Locate and identify every blood parasite.
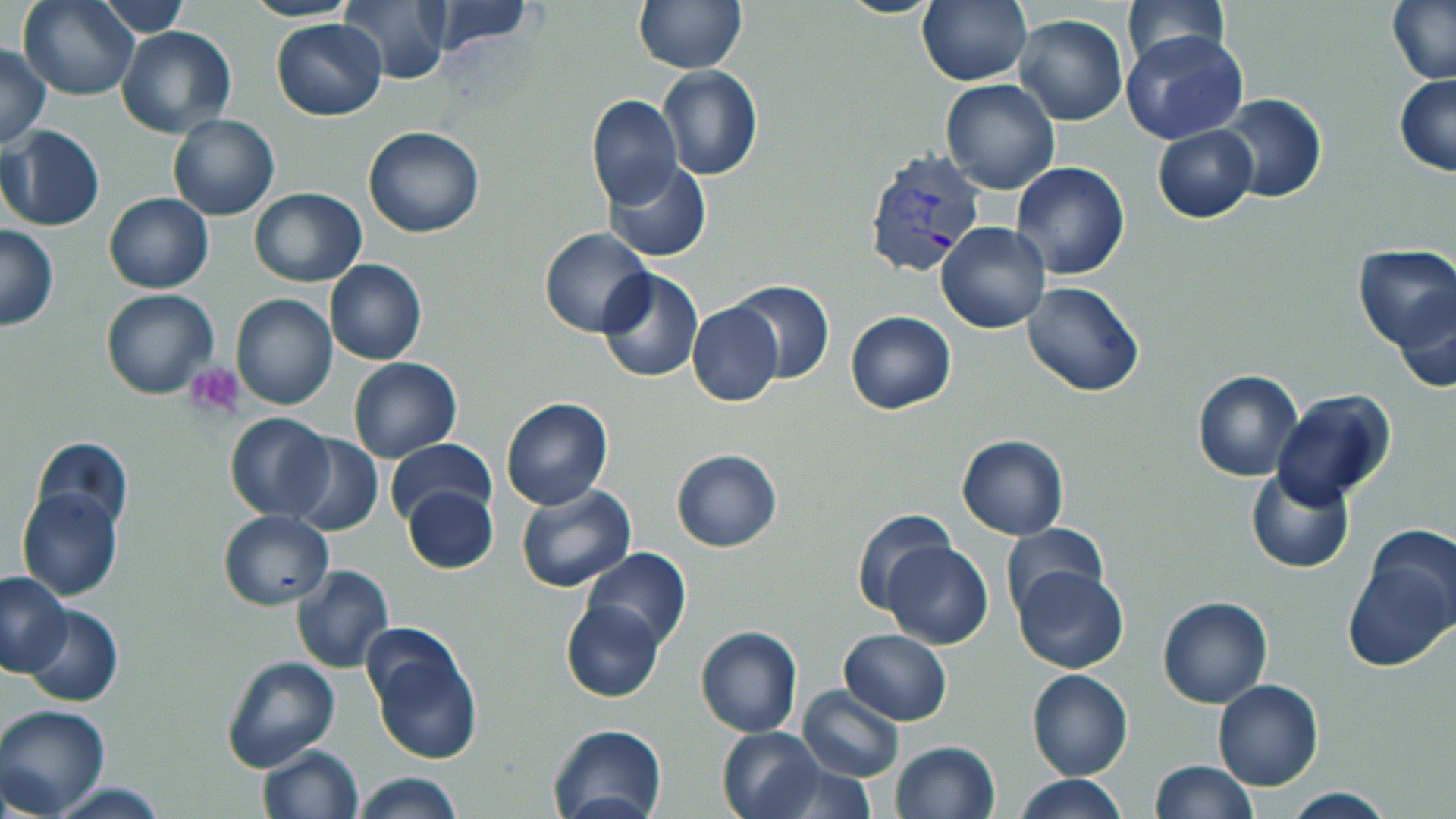

Approximate bounding boxes as (x1,y1)-(x2,y2) corner pairs in pixels.
Plasmodium vivax-infected red blood cells: (859,150)-(984,280).
No Plasmodium falciparum, Plasmodium ovale, Plasmodium malariae, Babesia divergens, or Trypanosoma brucei observed.

slide_level_diagnosis: Plasmodium vivax
magnification: 1000x
field_of_view: single
modality: light microscopy
preparation: thin blood film
uninfected_red_blood_cell_locations: 'approximate bounding boxes as (x1,y1)-(x2,y2) corner pairs in pixels: (20,0)-(140,100), (98,0)-(193,35), (243,0)-(359,24), (338,0)-(450,84), (835,0)-(944,18), (917,0)-(1031,86), (1122,0)-(1228,69), (1388,0)-(1456,86), (420,1)-(534,57), (633,1)-(745,73), (1014,13)-(1127,126), (271,18)-(387,121), (116,26)-(237,139), (1123,29)-(1248,145), (0,45)-(50,149), (658,65)-(763,181), (1395,75)-(1456,177), (940,77)-(1060,196), (1212,93)-(1327,203), (585,94)-(684,209), (168,114)-(279,221), (1152,124)-(1258,223), (1,125)-(104,233), (363,125)-(486,238), (604,159)-(712,263), (1011,161)-(1130,280), (248,187)-(367,286), (103,193)-(213,293), (935,222)-(1051,334), (0,225)-(58,331), (539,228)-(653,338), (1353,245)-(1456,351), (325,258)-(427,365), (596,268)-(704,383), (729,279)-(834,384), (1023,282)-(1145,399), (1394,288)-(1456,394), (101,289)-(218,399), (231,293)-(338,410), (686,302)-(782,406), (845,310)-(956,416), (347,358)-(461,462), (1192,369)-(1304,482), (1271,390)-(1397,505), (500,396)-(613,510), (224,414)-(335,522), (287,434)-(383,537), (957,435)-(1069,540), (30,436)-(133,533), (385,438)-(495,527), (671,449)-(780,552), (1245,465)-(1355,573), (514,484)-(637,595), (402,486)-(498,575), (16,487)-(123,601), (849,507)-(956,614), (218,510)-(335,610), (1001,523)-(1108,618), (1348,525)-(1456,671), (882,541)-(994,650), (585,547)-(690,652), (291,564)-(393,674), (1011,566)-(1127,675), (0,572)-(72,676), (1157,595)-(1272,708), (561,601)-(665,701), (20,603)-(123,708), (695,625)-(803,738), (838,629)-(953,725), (366,630)-(484,766), (221,655)-(342,773), (1026,669)-(1133,781), (1213,678)-(1324,791), (797,685)-(904,782), (0,705)-(112,818), (548,723)-(668,819), (717,726)-(826,819), (890,740)-(1000,819), (256,744)-(364,819), (1151,760)-(1257,818), (351,773)-(464,818), (1014,775)-(1126,818), (44,781)-(172,818), (1282,787)-(1397,818)'
image_size: 1456×819 pixels
stain: May-Grünwald-Giemsa
platelet_locations: 'approximate bounding boxes as (x1,y1)-(x2,y2) corner pairs in pixels: (184,367)-(247,419)'